State the blood parasite species.
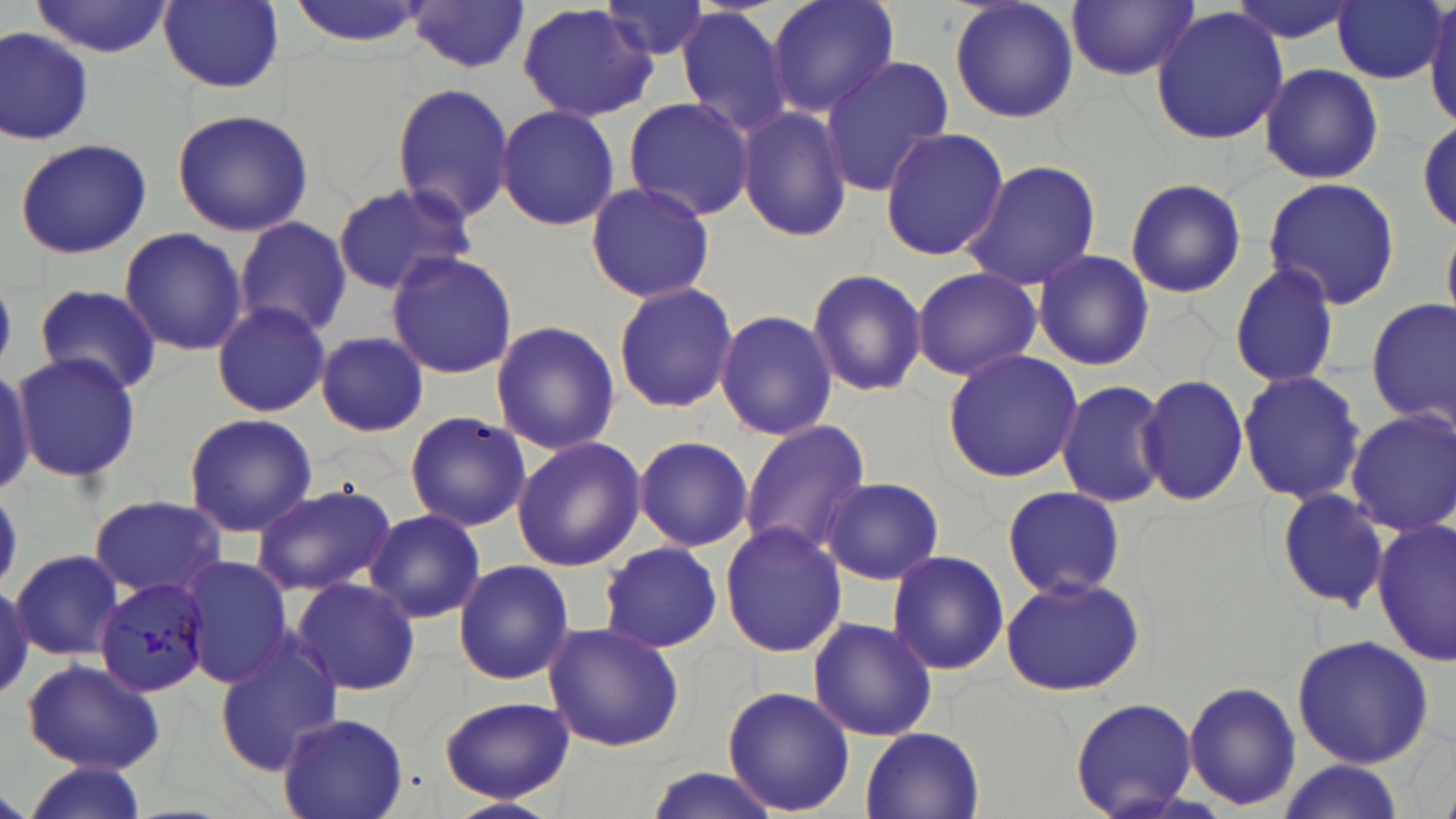
Plasmodium malariae.

modality: light microscopy
field_of_view: one of a larger specimen
preparation: thin blood smear
image_size: 1456×819 pixels
plasmodium_malariae_infected_red_blood_cell_locations: 'approximate bounding boxes as (x1,y1)-(x2,y2) corner pairs in pixels: (95,577)-(213,698)'
magnification: 1000x
stain: May-Grünwald-Giemsa
uninfected_red_blood_cell_locations: 'approximate bounding boxes as (x1,y1)-(x2,y2) corner pairs in pixels: (285,0)-(432,49), (765,0)-(901,121), (949,0)-(1079,124), (1068,0)-(1197,80), (1223,0)-(1364,45), (32,1)-(174,58), (602,1)-(719,66), (1332,1)-(1446,85), (407,2)-(529,75), (159,3)-(286,93), (516,3)-(661,122), (675,5)-(795,139), (1426,5)-(1456,125), (1150,7)-(1288,144), (1,27)-(94,146), (818,57)-(955,195), (1259,63)-(1384,185), (391,82)-(516,225), (620,98)-(756,220), (495,104)-(621,231), (737,105)-(852,242), (172,108)-(314,236), (1414,112)-(1455,236), (878,126)-(1010,262), (14,137)-(153,260), (961,160)-(1102,289), (1262,175)-(1400,311), (1124,176)-(1247,299), (586,178)-(716,304), (332,181)-(477,297), (232,217)-(354,339), (119,228)-(248,357), (385,249)-(518,378), (1033,249)-(1155,371), (1229,260)-(1341,390), (911,265)-(1042,381), (805,268)-(927,398), (612,280)-(739,414), (34,284)-(161,394), (1367,298)-(1455,428), (211,301)-(332,416), (714,309)-(837,440), (489,320)-(621,454), (315,331)-(430,437), (12,350)-(141,483), (942,350)-(1082,484), (0,364)-(34,493), (1237,371)-(1365,504), (1136,374)-(1248,504), (1056,381)-(1169,507), (1346,408)-(1456,535), (403,411)-(529,533), (180,412)-(318,538), (739,420)-(872,558), (510,435)-(646,572), (633,435)-(754,552), (820,476)-(944,584), (249,480)-(398,597), (1000,486)-(1129,601), (1275,487)-(1391,611), (87,495)-(227,601), (366,509)-(485,623), (1373,519)-(1454,664), (720,522)-(847,657), (599,540)-(724,653), (11,548)-(125,660), (887,550)-(1010,677), (178,556)-(297,688), (453,559)-(575,685), (999,573)-(1145,697), (289,576)-(420,698), (808,616)-(939,741), (542,622)-(685,753), (1291,634)-(1434,768), (213,638)-(344,775), (23,658)-(163,772), (1183,679)-(1302,810), (723,683)-(854,816), (1069,695)-(1199,818), (436,696)-(577,803), (277,714)-(409,819), (857,725)-(986,819), (1272,760)-(1405,819), (21,762)-(149,817), (638,767)-(785,819), (446,797)-(560,819)'